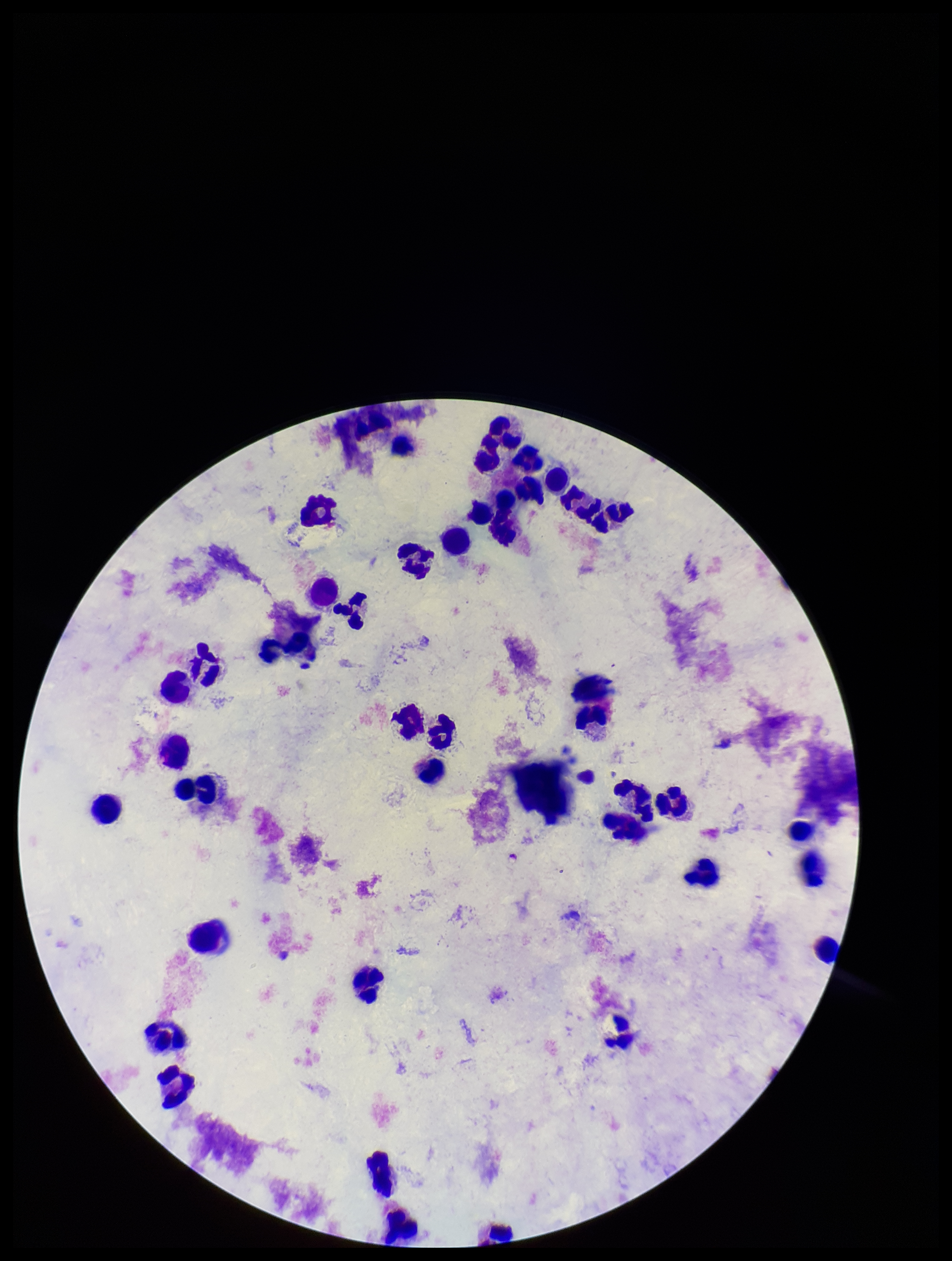

Photographed through the microscope eyepiece with a smartphone camera. Parasite count: 0. Single field of view. Plasmodium parasites: none seen. Giemsa stain. Preparation: thick smear. Image is 952×1261 pixels. Leukocyte count: 36. Patient malaria status: negative.